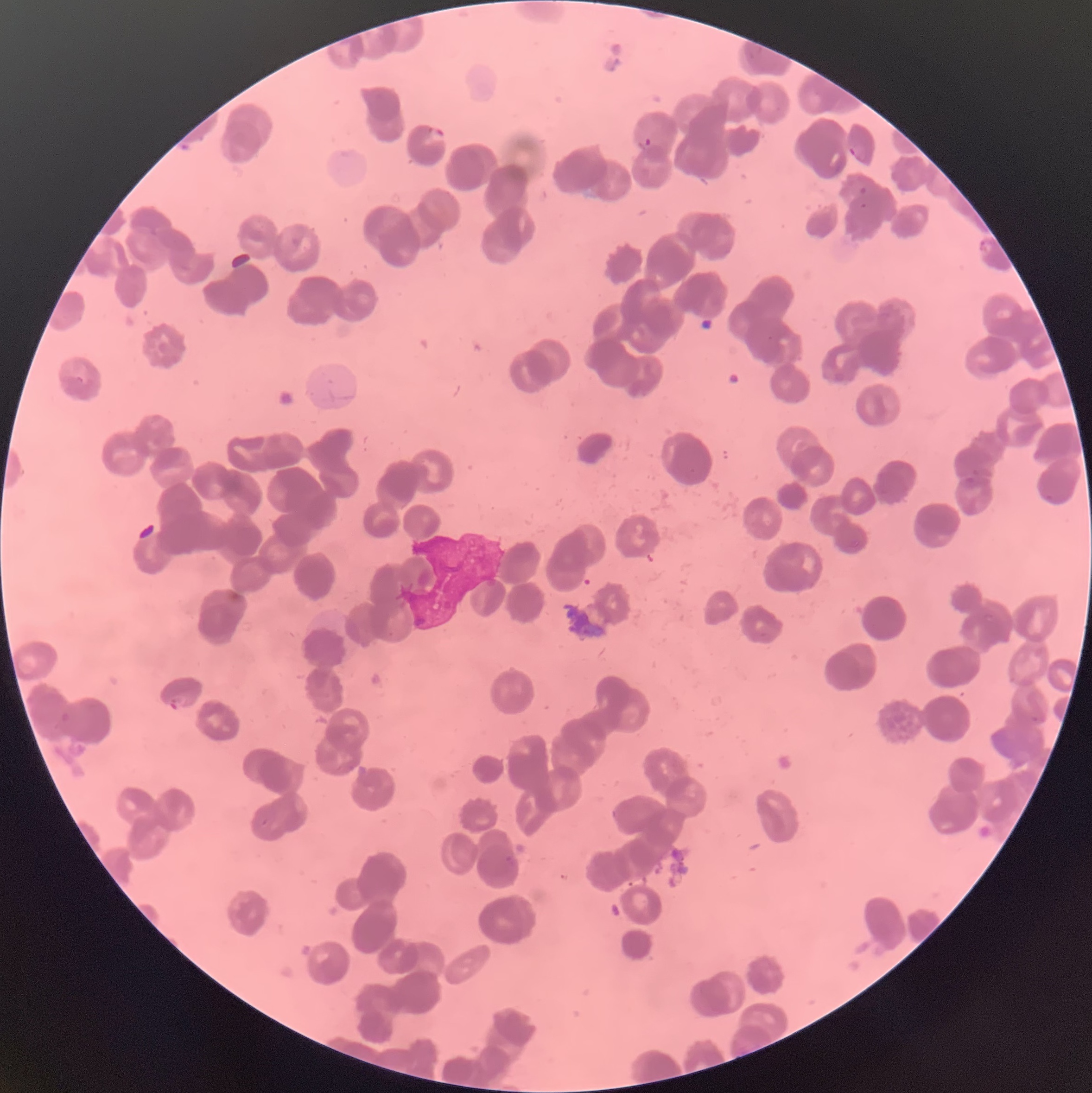
Summary:
  - Coordinate format: approximate bounding boxes as (x1,y1)-(x2,y2) corner pairs in pixels
  - Plasmodium parasite locations: (743,44)-(761,61), (428,129)-(447,144), (645,137)-(652,146), (848,146)-(867,163), (860,187)-(867,196), (979,239)-(993,258), (972,469)-(984,475), (963,475)-(977,485), (1043,493)-(1058,503), (168,694)-(187,710), (61,712)-(70,723), (1029,716)-(1041,725), (505,854)-(516,868)
  - Plasmodium parasites too small for a box (approximate centers as (x,y) in pixels): (863,205), (771,338)
  - Preparation: thin blood film
  - Image size: 1092×1093 pixels
  - Modality: optical microscopy
  - Red blood cell morphology: rouleaux formation